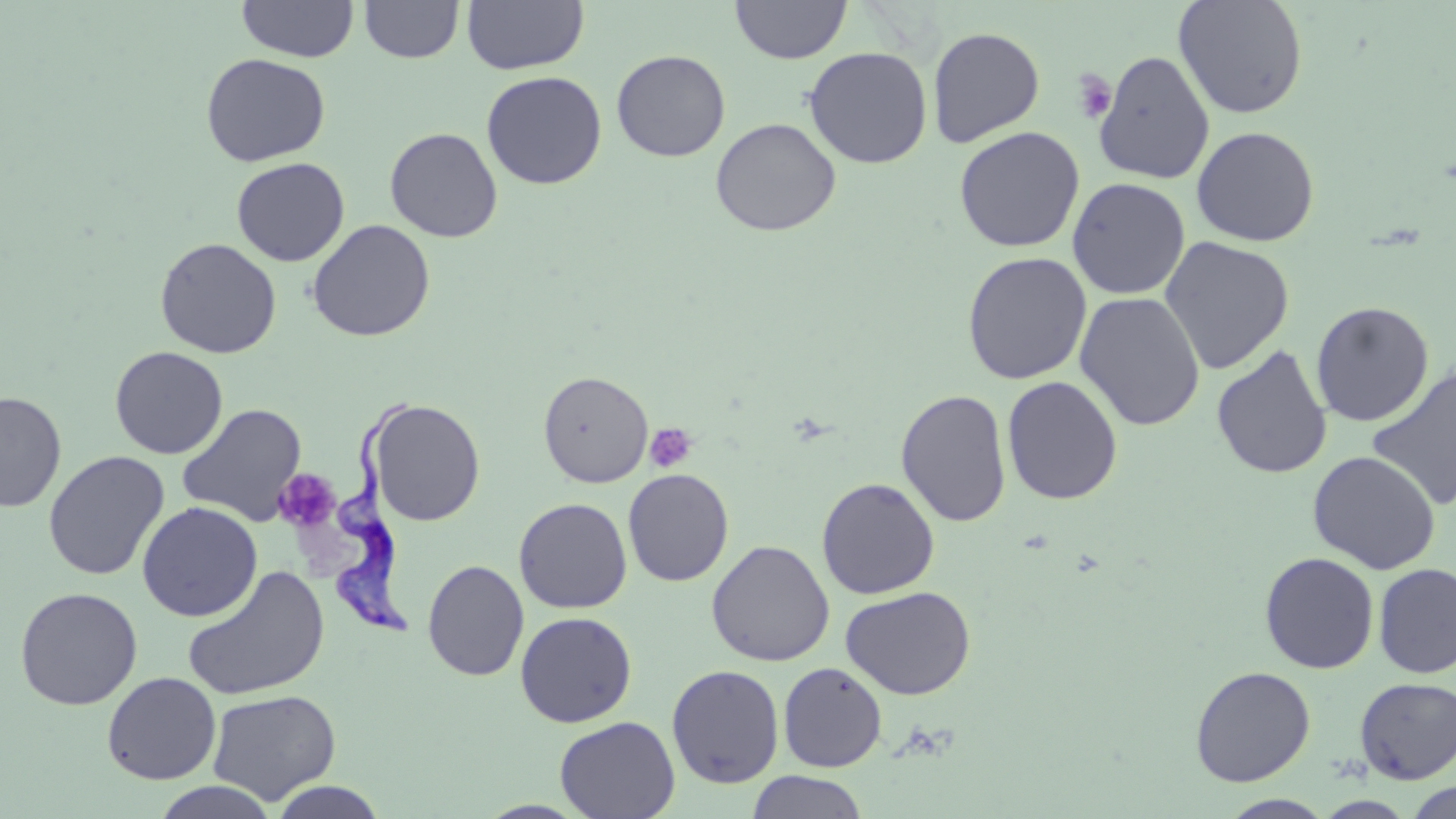
Summary:
  - Coordinate format: approximate bounding boxes as (x1, y1, x2, y2) in pixels
  - Platelet locations: (1071, 70, 1117, 125), (645, 423, 696, 473), (275, 468, 341, 532)
  - Uninfected red blood cell locations: (238, 0, 357, 62), (360, 0, 464, 63), (462, 0, 589, 75), (730, 0, 851, 64), (1173, 0, 1309, 119), (927, 26, 1046, 148), (803, 46, 933, 169), (1093, 49, 1215, 185), (611, 50, 731, 161), (200, 52, 331, 167), (481, 70, 607, 190), (709, 117, 842, 237), (1191, 125, 1320, 247), (954, 126, 1085, 253), (384, 127, 503, 243), (231, 157, 350, 267), (1067, 177, 1190, 300), (308, 219, 435, 341), (1158, 236, 1295, 374), (155, 237, 282, 359), (961, 251, 1092, 385), (1074, 290, 1206, 431), (1310, 301, 1434, 427), (1211, 344, 1333, 479), (110, 346, 228, 459), (1365, 364, 1456, 513), (538, 370, 653, 487), (1001, 376, 1123, 505), (895, 388, 1012, 527), (0, 390, 67, 512), (367, 399, 486, 526), (177, 403, 308, 526), (1308, 450, 1440, 574), (43, 451, 169, 581), (622, 468, 734, 586), (816, 477, 940, 599), (827, 478, 957, 703), (514, 497, 632, 613), (137, 501, 262, 622), (706, 539, 834, 666), (1259, 551, 1380, 674), (422, 559, 529, 681), (1373, 562, 1456, 679), (182, 565, 330, 702), (840, 585, 976, 700), (15, 587, 143, 710), (515, 611, 637, 727), (778, 662, 887, 772), (666, 664, 784, 788), (1190, 665, 1316, 786), (102, 671, 221, 785), (1355, 677, 1456, 784), (207, 689, 341, 805), (554, 715, 680, 819), (746, 770, 869, 819), (267, 780, 388, 819), (1404, 780, 1456, 818), (150, 781, 280, 819), (1219, 794, 1336, 818)
  - Trypanosoma brucei locations: (328, 390, 421, 644)
  - Slide-level diagnosis: Trypanosoma brucei
  - Image size: 1456×819 pixels
  - Modality: light microscopy
  - Stain: May-Grünwald-Giemsa
  - Preparation: thin blood smear
  - Field of view: one of a larger specimen
  - Magnification: 1000x